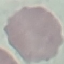

{
  "result": "no malaria parasites seen",
  "preparation": "thin blood film",
  "image_type": "cell patch, automatically extracted from a larger field of view and resized to 64 × 64 pixels",
  "capture": "smartphone camera at the microscope eyepiece",
  "stain": "Giemsa"
}